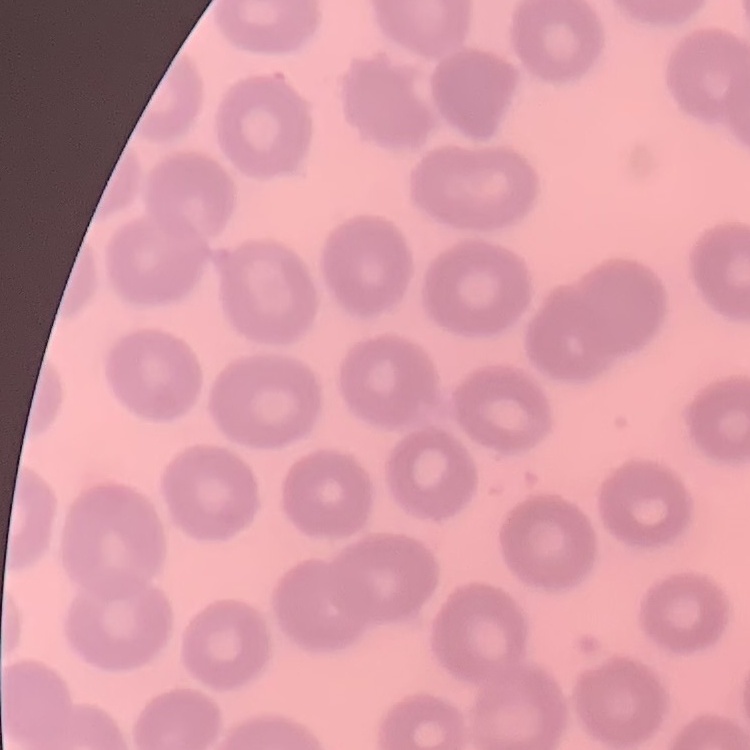

Summary:
  - Red blood cell morphology: no rouleaux formation
  - Stain: Field's or Giemsa
  - Image type: square crop of a larger photomicrograph
  - Preparation: thin blood film